Report the malaria status.
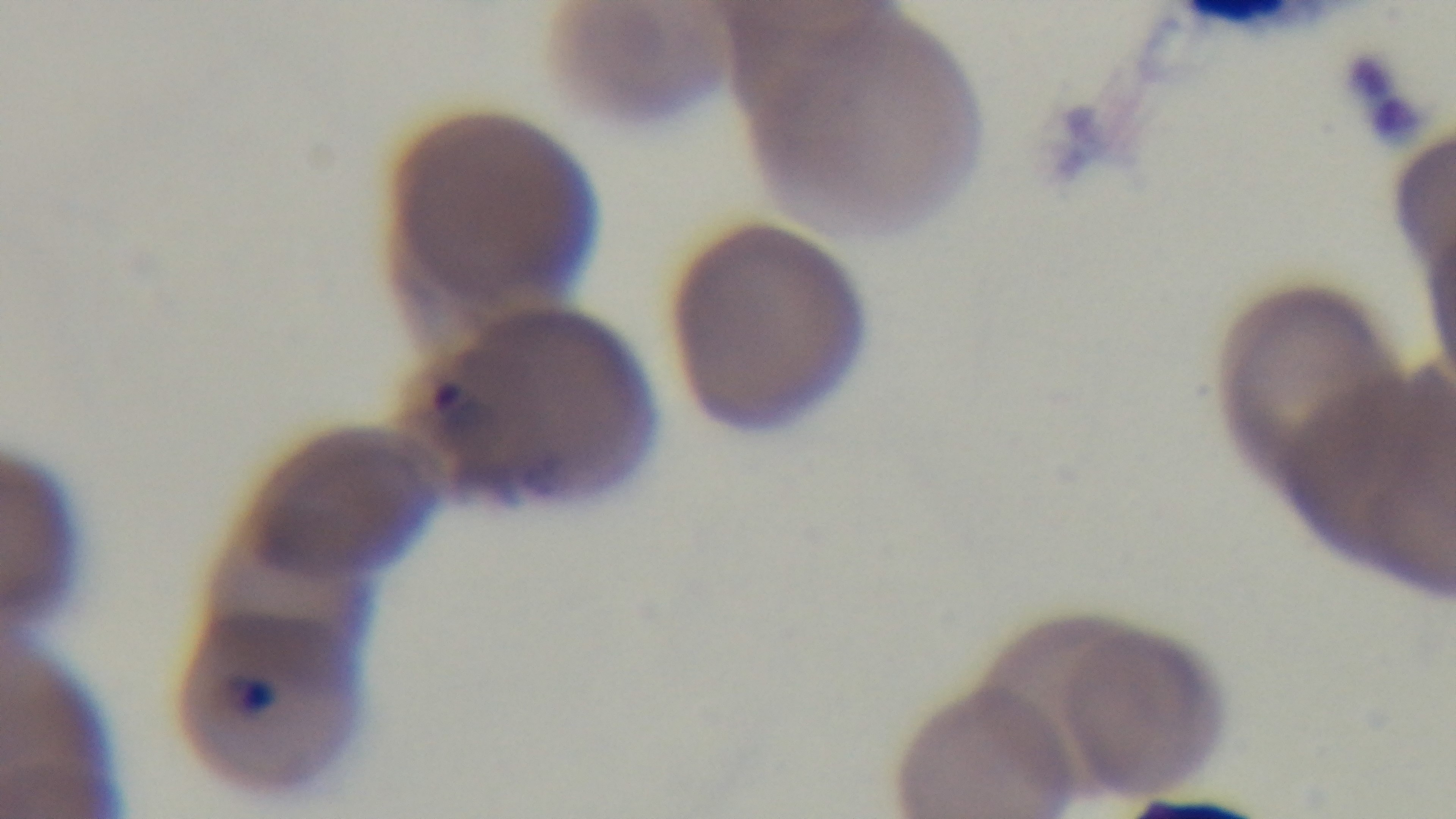

It is infected.

Summary:
  - Field of view: single
  - Objective: 100x oil immersion
  - Preparation: thin
  - Capture: mounted 4K digital camera
  - Stain: Giemsa
  - Modality: light microscopy